Identify the parasite.
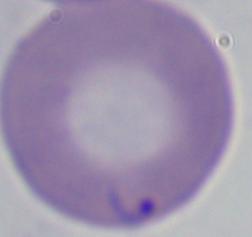

This is Babesia.

Micrograph. 1000x magnification.